Locate every Plasmodium parasite and every leukocyte.
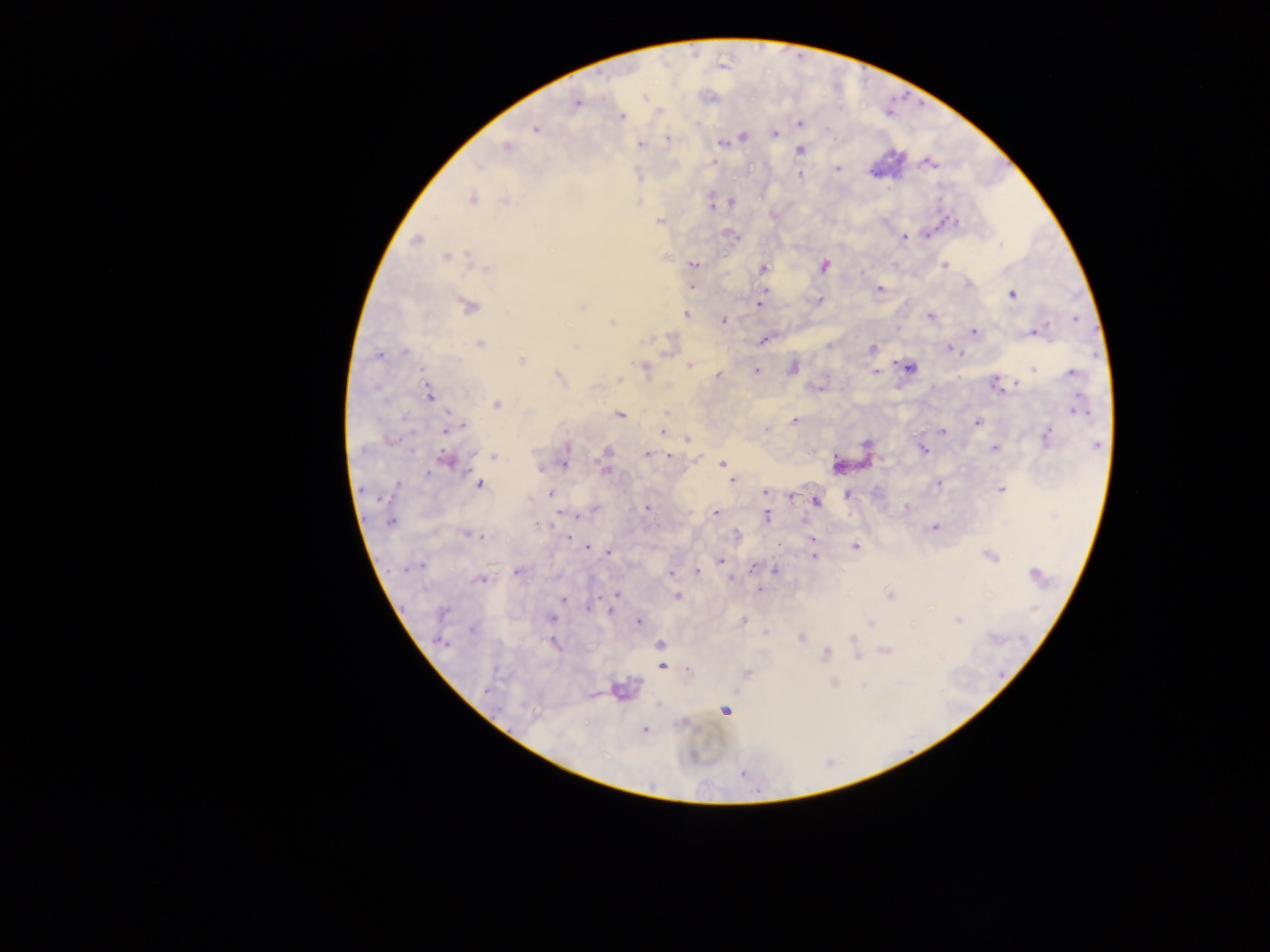

Approximate centers as {x, y} in pixels.
Plasmodium parasites: {646, 98}, {576, 103}, {620, 116}, {799, 122}, {536, 128}, {774, 133}, {742, 137}, {667, 139}, {722, 142}, {639, 144}, {507, 147}, {799, 150}, {715, 162}, {930, 163}, {837, 169}, {799, 174}, {471, 199}, {505, 200}, {730, 202}, {710, 205}, {660, 220}, {950, 221}, {903, 237}, {416, 240}, {447, 257}, {693, 265}, {945, 265}, {822, 266}, {483, 268}, {764, 268}, {969, 283}, {692, 287}, {764, 289}, {879, 289}, {1013, 294}, {819, 301}, {467, 305}, {759, 305}, {686, 313}, {931, 316}, {723, 320}, {612, 322}, {973, 331}, {1037, 331}, {764, 338}, {479, 344}, {575, 346}, {871, 349}, {951, 349}, {377, 354}, {520, 361}, {689, 366}, {908, 367}, {1033, 367}, {792, 368}, {645, 369}, {757, 370}, {876, 371}, {1073, 372}, {718, 375}, {560, 378}, {996, 383}, {429, 394}, {497, 405}, {1077, 409}, {619, 414}, {794, 421}, {977, 422}, {451, 428}, {662, 431}, {942, 431}, {1046, 437}, {687, 440}, {567, 449}, {995, 449}, {923, 450}, {606, 451}, {646, 454}, {493, 455}, {669, 455}, {564, 457}, {445, 460}, {723, 463}, {837, 465}, {605, 469}, {733, 480}, {937, 482}, {478, 484}, {1000, 489}, {765, 492}, {551, 494}, {791, 495}, {848, 495}, {815, 500}, {906, 507}, {646, 508}, {715, 513}, {577, 515}, {765, 516}, {390, 521}, {934, 527}, {468, 534}, {568, 537}, {812, 539}, {778, 543}, {854, 546}, {587, 547}, {607, 551}, {990, 555}, {813, 556}, {719, 560}, {418, 566}, {752, 568}, {518, 570}, {695, 571}, {774, 571}, {670, 574}, {1035, 574}, {732, 578}, {481, 579}, {759, 590}, {617, 595}, {890, 595}, {677, 597}, {562, 599}, {587, 607}, {551, 618}, {638, 621}, {742, 621}, {957, 621}, {869, 622}, {472, 629}, {802, 638}, {442, 642}, {553, 643}, {660, 645}, {885, 651}, {825, 654}, {857, 655}, {660, 657}, {661, 665}, {687, 670}, {745, 673}, {619, 690}, {724, 711}, {644, 730}.
No leukocytes observed.

Summary:
  - Preparation: thick blood smear
  - Image size: 1270×952 pixels
  - Field of view: single
  - Capture: mobile-phone photograph through a microscope
  - Country: Ghana